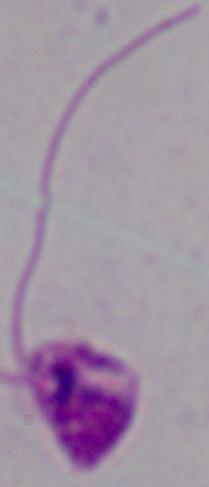

Micrograph. A Leishmania parasite is shown. Captured at 1000x magnification.